Assess this cell for malaria.
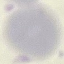

Uninfected.

Summary:
  - Image type: cell patch, automatically extracted from a larger field of view and resized to 64 × 64 pixels
  - Preparation: thin blood smear
  - Stain: Giemsa
  - Capture: smartphone through the microscope eyepiece